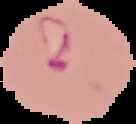 Segmented cell region on a black background. Image is 136×124 pixels. From a thin blood smear. Malaria status: parasitized.